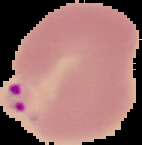 The area outside the segmented cell region is set to black. Image is 142×145 pixels. Result: malaria parasites identified. From a thin blood film.